Locate every Plasmodium ovale-infected red blood cell.
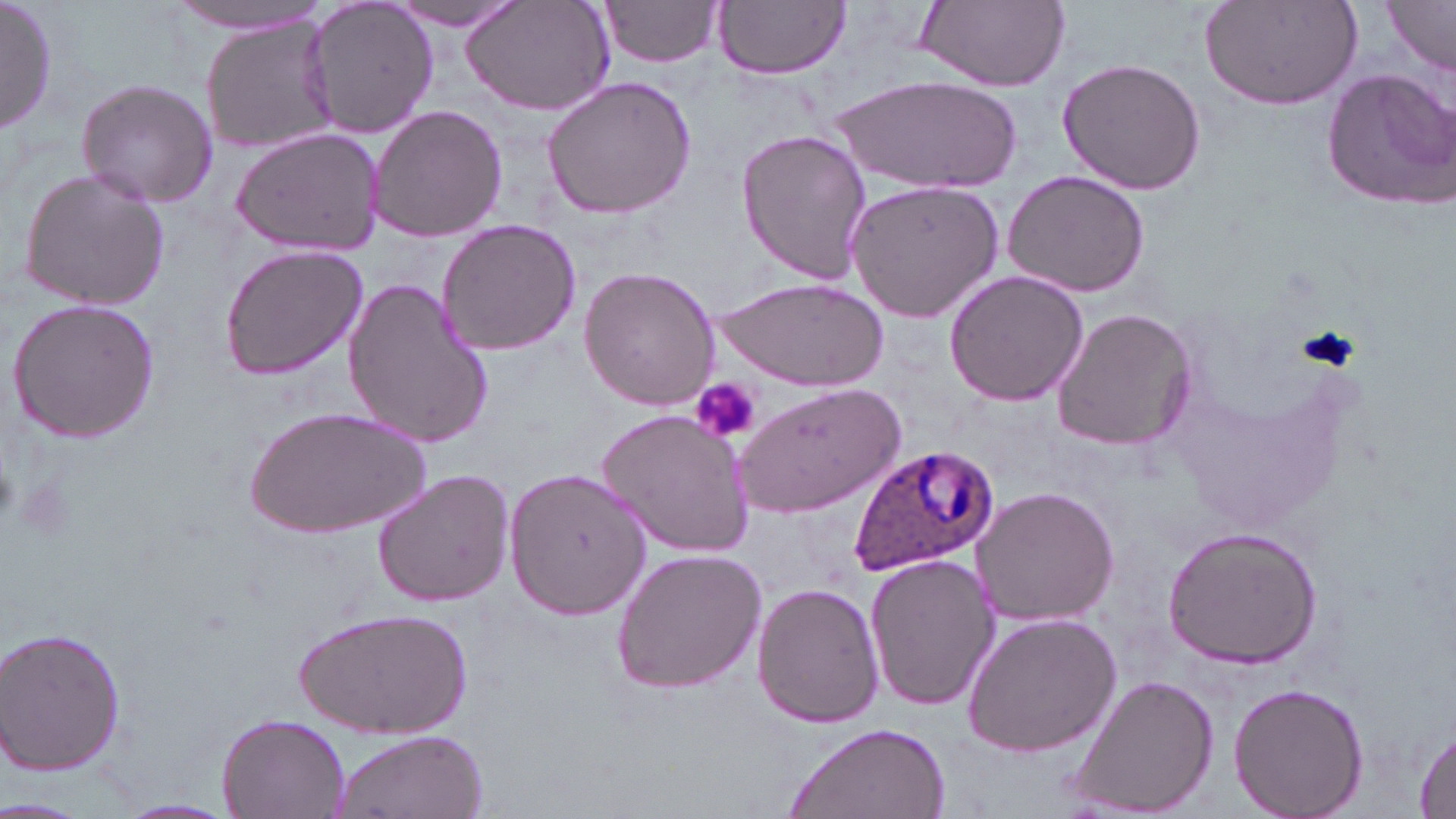

Approximate bounding boxes as (x1, y1, x2, y2) in pixels.
Plasmodium ovale-infected red blood cells: (846, 442, 1000, 578).

Uninfected red blood cell locations: (1, 0, 56, 138), (300, 0, 440, 139), (459, 0, 617, 117), (599, 0, 726, 68), (716, 0, 850, 80), (916, 0, 1071, 90), (1199, 0, 1367, 111), (162, 1, 330, 35), (389, 1, 526, 35), (1386, 1, 1456, 73), (200, 15, 339, 156), (1056, 57, 1208, 196), (1321, 66, 1456, 210), (539, 74, 698, 221), (835, 74, 1025, 191), (74, 77, 219, 209), (366, 104, 508, 244), (230, 125, 385, 256), (736, 128, 874, 284), (16, 167, 171, 311), (1002, 171, 1151, 298), (843, 181, 1005, 324), (435, 218, 584, 357), (218, 243, 370, 381), (578, 267, 721, 411), (943, 269, 1089, 407), (341, 276, 495, 450), (716, 276, 888, 389), (7, 298, 162, 443), (1053, 307, 1197, 451), (732, 380, 907, 518), (250, 404, 428, 541), (595, 408, 756, 559), (504, 465, 652, 619), (372, 468, 516, 609), (972, 487, 1119, 627), (1161, 525, 1324, 669), (609, 547, 768, 695), (864, 552, 998, 712), (751, 583, 884, 729), (300, 605, 467, 738), (959, 613, 1122, 757), (2, 625, 128, 776), (1069, 677, 1219, 816), (1229, 682, 1368, 818), (216, 711, 350, 819), (786, 722, 952, 819), (1412, 723, 1456, 819), (327, 728, 487, 819), (0, 797, 86, 818), (115, 798, 239, 818). Platelet locations: (1297, 325, 1360, 373), (693, 379, 761, 443), (0, 456, 18, 524), (16, 477, 77, 544). Slide-level diagnosis: Plasmodium ovale. Image is 1456×819 pixels. Thin blood film. May-Grünwald-Giemsa stain. One field of a larger specimen. Light microscopy. Captured at 1000x magnification.